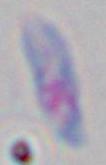 Photomicrograph. 1000x magnification. Toxoplasma gondii is seen.